Report the malaria status.
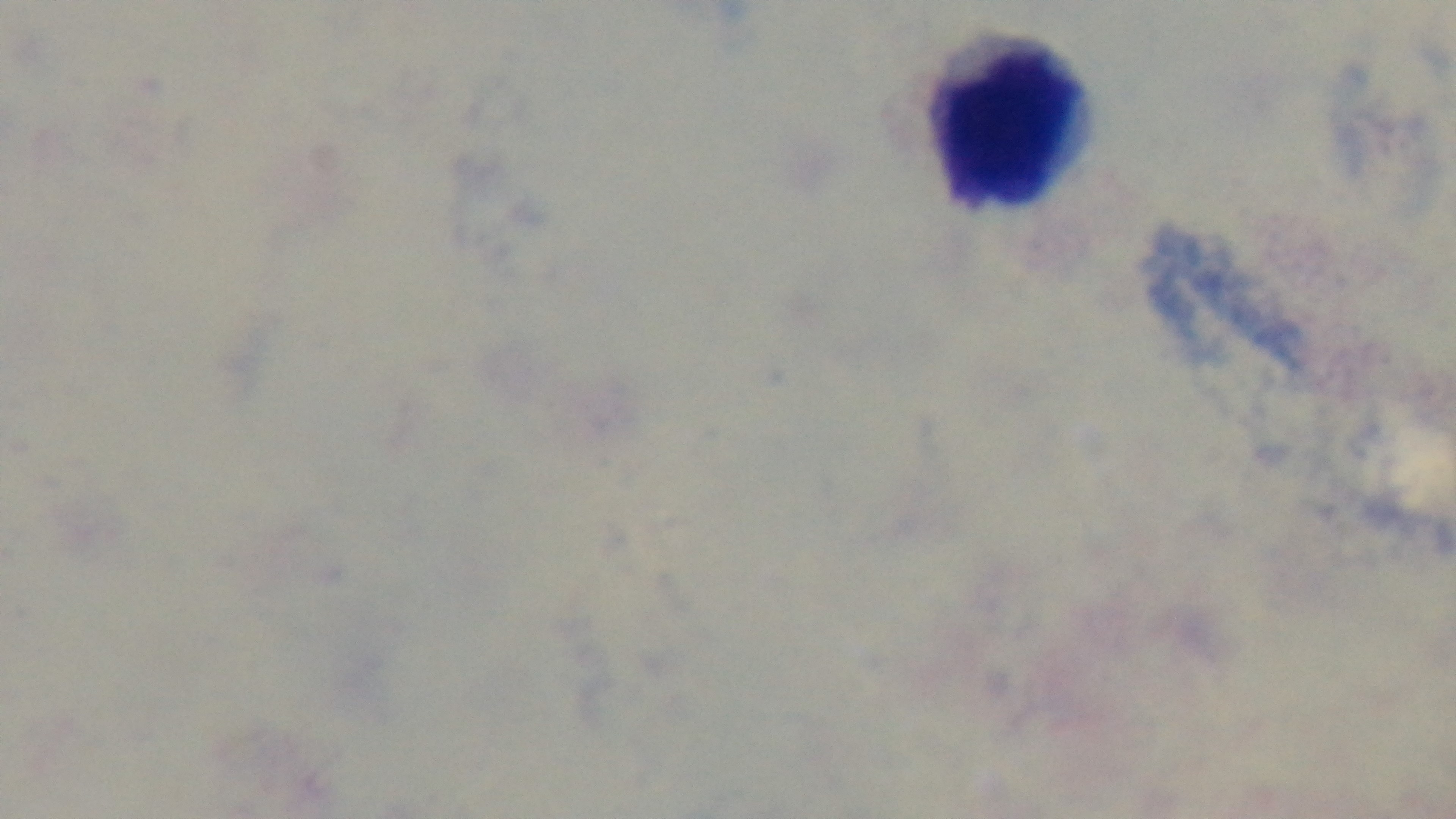
Negative.

stain = Giemsa
objective = 100x oil immersion
field of view = one from the slide
capture = mounted 4K digital camera
modality = light microscopy
preparation = thick